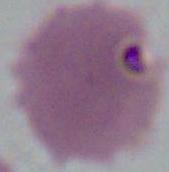

Micrograph. Captured at 1000x magnification. A red blood cell is shown.